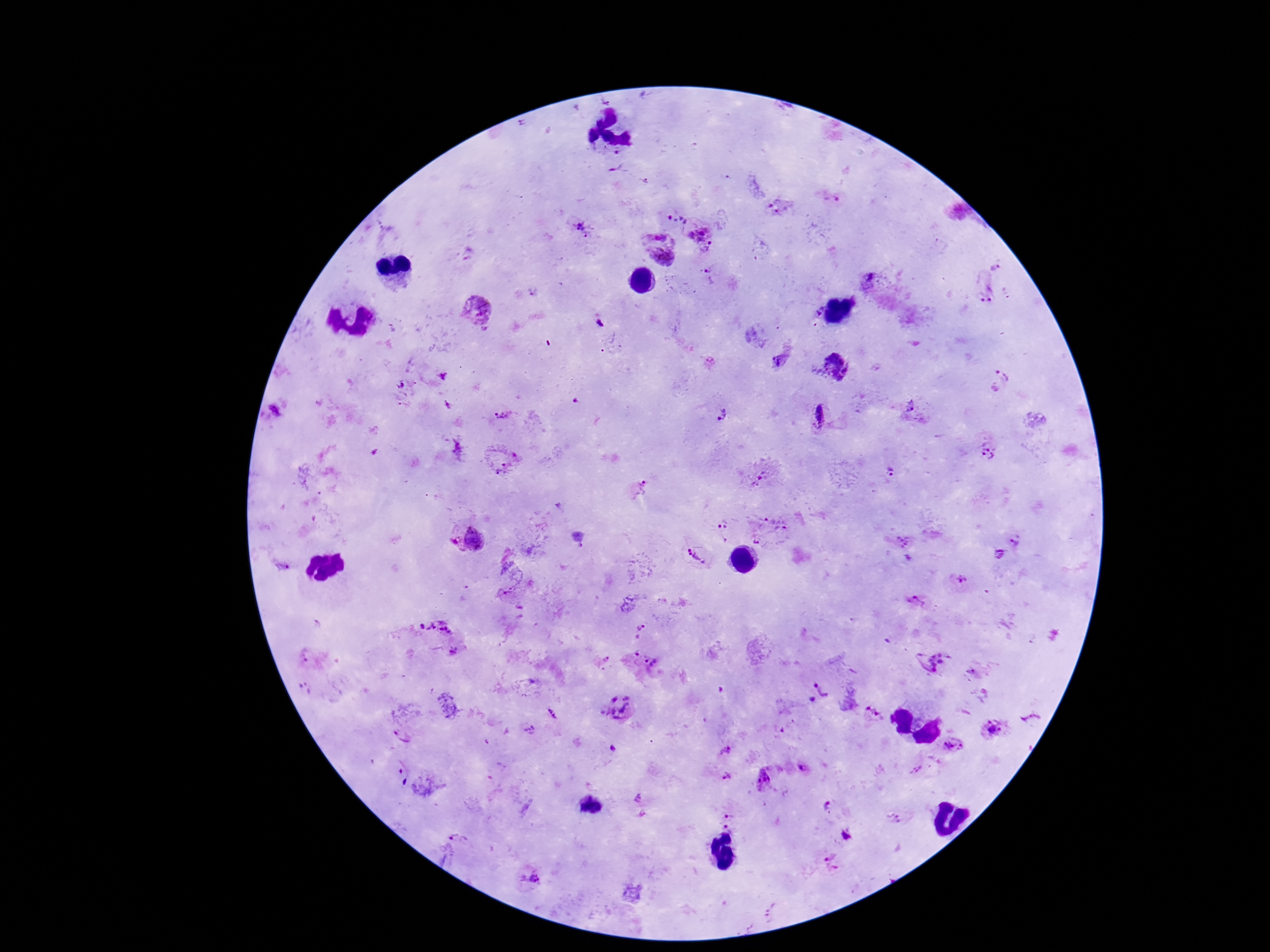 Approximate centers as [x, y] in pixels. Plasmodium parasite locations: [621, 173], [831, 198], [780, 205], [676, 220], [585, 225], [704, 233], [661, 248], [998, 265], [711, 275], [989, 291], [480, 309], [599, 321], [779, 360], [831, 367], [442, 376], [998, 381], [405, 384], [403, 405], [448, 405], [906, 406], [277, 410], [722, 415], [501, 416], [819, 416], [458, 449], [985, 452], [503, 459], [891, 472], [762, 479], [638, 492], [777, 521], [724, 531], [476, 540], [1018, 540], [906, 546], [1001, 555], [698, 557], [960, 581], [917, 603], [437, 626], [640, 632], [454, 651], [309, 655], [602, 661], [933, 661], [642, 662], [972, 674], [304, 689], [818, 692], [620, 706], [554, 714], [872, 714], [992, 728], [530, 729], [404, 733], [952, 745], [612, 749], [724, 752], [804, 768], [918, 769], [764, 776], [728, 777], [640, 806], [827, 806], [729, 810], [894, 819], [732, 828], [846, 834], [832, 861], [530, 879], [773, 903], [766, 920]. Smartphone photograph taken through the microscope eyepiece. 100x magnification. Single field of view. Patient malaria status: positive. Thick blood film. Image is 1270×952 pixels. Giemsa-stained preparation.